Identify the parasite.
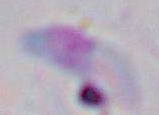

Toxoplasma gondii.

{
  "modality": "photomicrograph",
  "magnification": "1000x"
}